Give the position of every Plasmodium parasite visible.
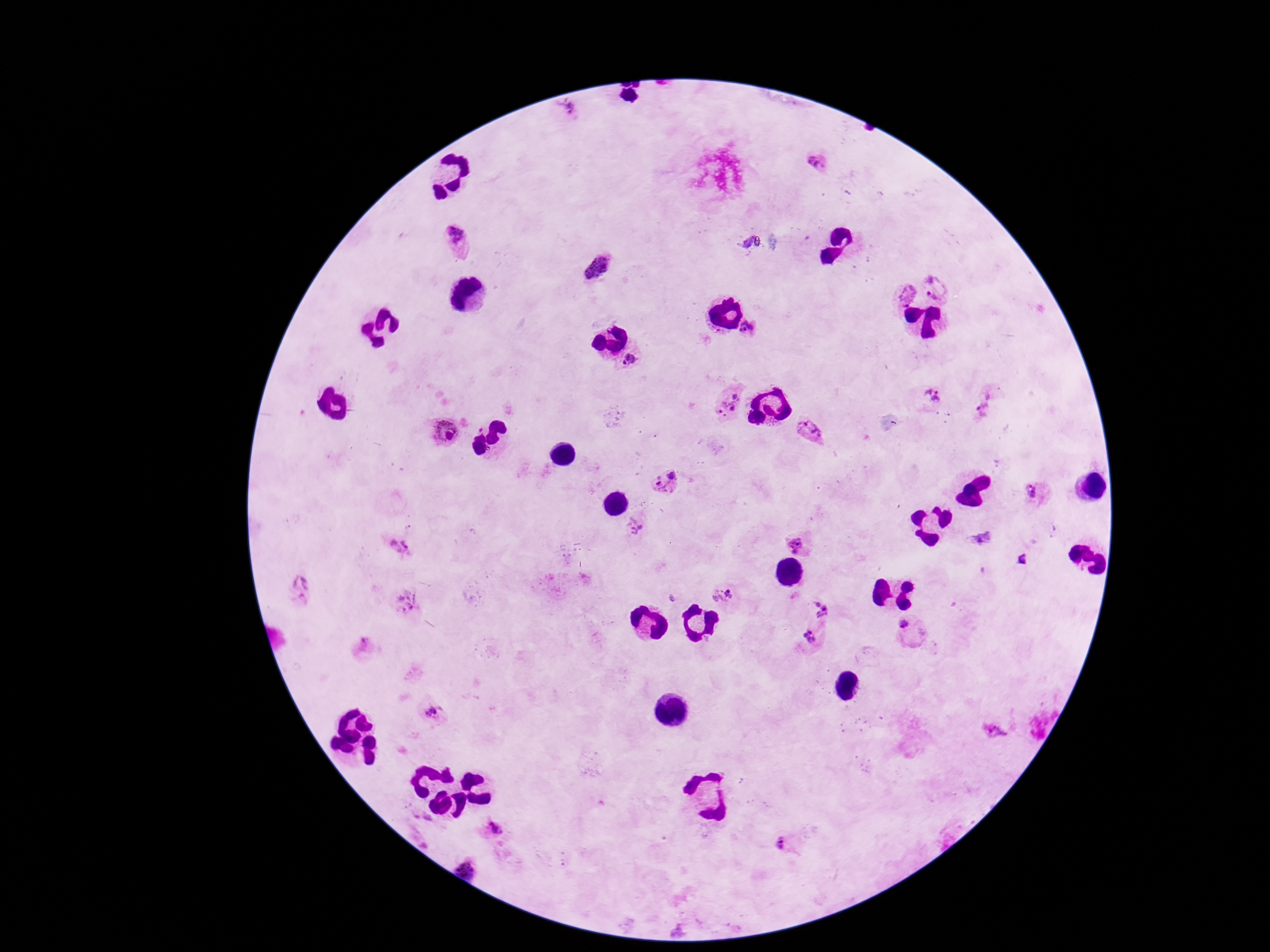

Approximate object centers, in pixels from the top-left corner.
Plasmodium parasites: (x=568, y=112), (x=814, y=162), (x=461, y=239), (x=600, y=268), (x=939, y=284), (x=901, y=294), (x=751, y=324), (x=631, y=361), (x=931, y=394), (x=725, y=398), (x=812, y=430), (x=441, y=433), (x=668, y=482), (x=1030, y=493), (x=633, y=525), (x=397, y=547), (x=798, y=547), (x=296, y=589), (x=724, y=591), (x=404, y=603), (x=823, y=606), (x=904, y=625), (x=812, y=636), (x=363, y=645), (x=430, y=712), (x=993, y=731), (x=495, y=834), (x=785, y=848), (x=467, y=869).

magnification: 100x
capture: smartphone camera through the microscope eyepiece
stain: Giemsa
preparation: thick blood smear
field_of_view: one from this slide
patient_malaria_status: positive
image_size: 1270×952 pixels